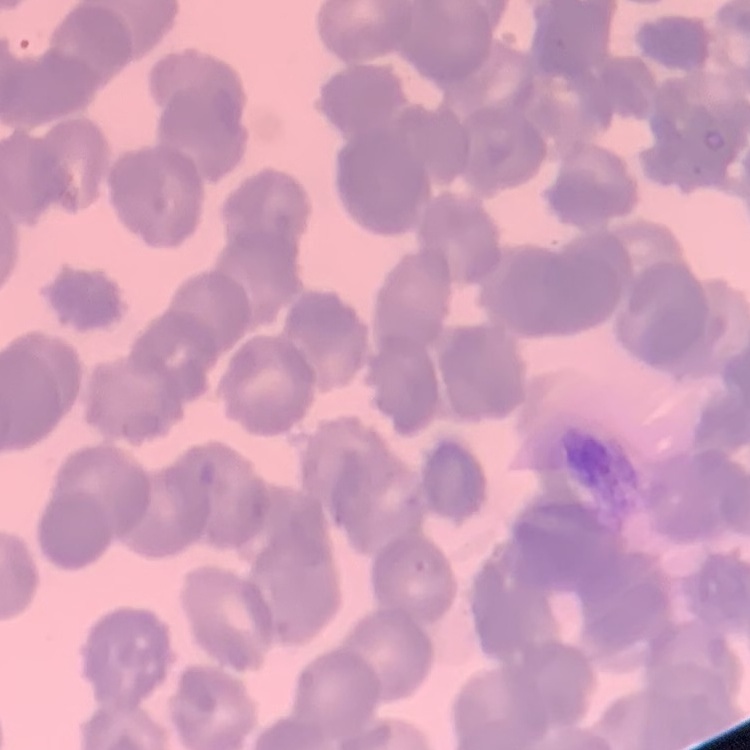
The erythrocytes exhibit rouleaux formation. Thin peripheral smear. Square crop of a larger photomicrograph. Stained with either Field's or Giemsa.